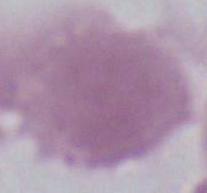

{
  "magnification": "1000x",
  "identification": "red blood cell",
  "modality": "photomicrograph"
}